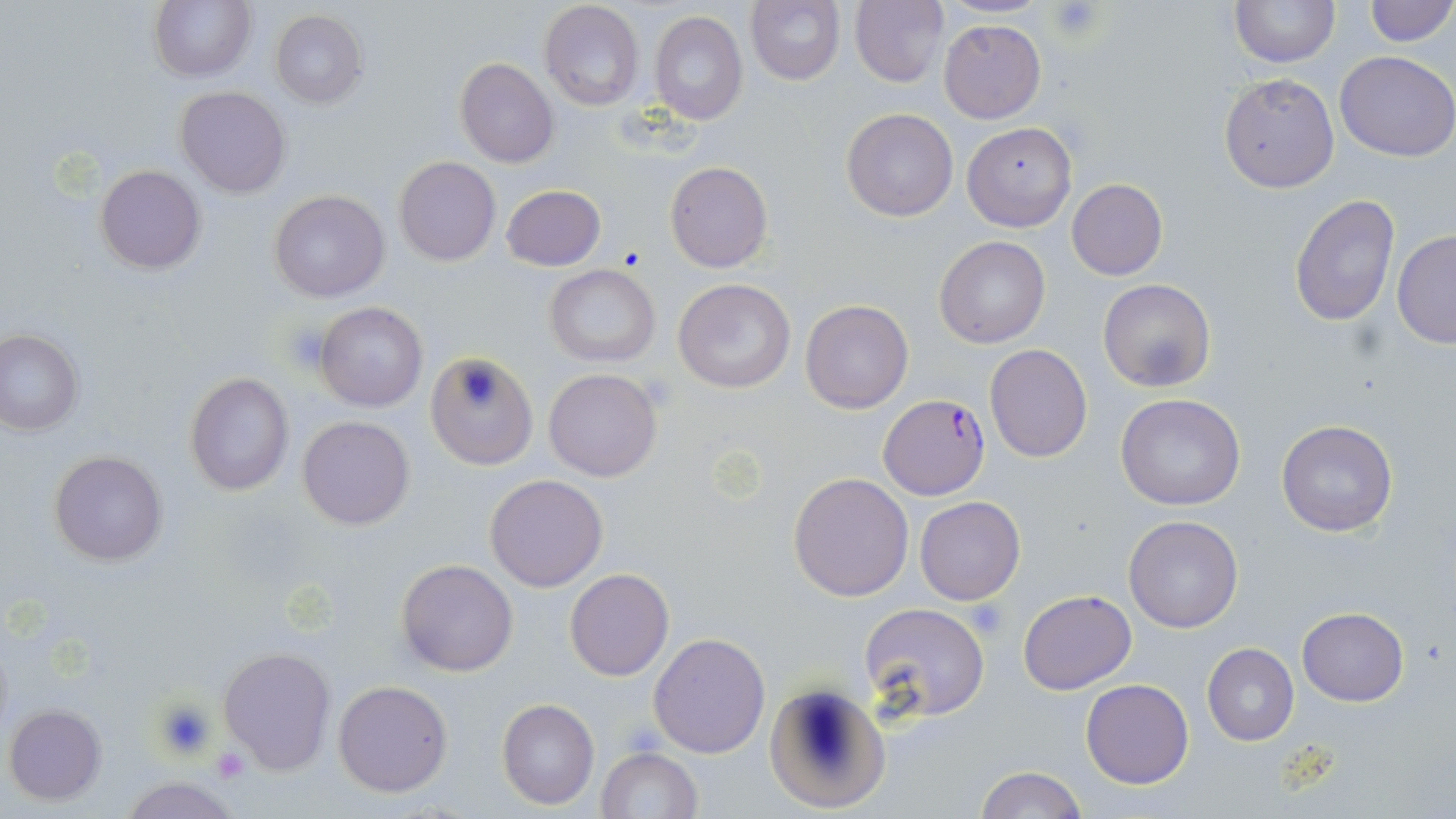
Approximate bounding boxes as [x1, y1, x2, y2] in pixels. Platelet locations: [1048, 1, 1104, 40], [280, 322, 333, 375], [968, 600, 1010, 640], [152, 697, 216, 761], [212, 745, 248, 780]. Uninfected red blood cell locations: [149, 0, 257, 83], [850, 0, 950, 88], [1229, 0, 1340, 68], [1362, 0, 1455, 47], [538, 1, 644, 112], [746, 1, 845, 86], [270, 9, 368, 108], [648, 11, 747, 125], [939, 18, 1046, 122], [1335, 50, 1456, 162], [454, 58, 559, 168], [1218, 72, 1339, 193], [175, 86, 290, 198], [842, 107, 959, 222], [962, 122, 1076, 231], [392, 156, 501, 267], [665, 160, 772, 273], [95, 165, 204, 275], [1066, 178, 1167, 280], [501, 184, 605, 271], [268, 189, 390, 302], [1289, 191, 1398, 327], [1392, 231, 1456, 349], [934, 235, 1050, 348], [545, 265, 660, 366], [672, 278, 796, 392], [1097, 278, 1216, 393], [800, 299, 913, 414], [314, 302, 428, 413], [1, 328, 84, 434], [984, 344, 1093, 462], [426, 351, 538, 469], [543, 367, 662, 482], [184, 373, 296, 496], [1115, 392, 1246, 512], [297, 415, 414, 530], [1277, 419, 1398, 537], [49, 450, 168, 567], [788, 473, 913, 602], [484, 474, 608, 592], [915, 496, 1025, 605], [1124, 514, 1244, 633], [395, 558, 520, 677], [564, 568, 674, 680], [1019, 590, 1137, 694], [859, 603, 991, 722], [1296, 608, 1408, 706], [647, 632, 771, 758], [1202, 643, 1299, 745], [218, 646, 336, 774], [1080, 678, 1195, 789], [334, 679, 453, 798], [761, 682, 890, 813], [496, 698, 600, 809], [4, 704, 106, 805], [596, 747, 703, 819], [972, 765, 1086, 819], [116, 776, 247, 819]. Plasmodium falciparum-infected red blood cell locations: [880, 395, 989, 498]. Slide-level diagnosis: Plasmodium falciparum. Thin blood film. Image is 1456×819 pixels. 1000x magnification. May-Grünwald-Giemsa-stained preparation. Single field of view. Optical microscopy.